Draw a bounding box around every parasitised red blood cell.
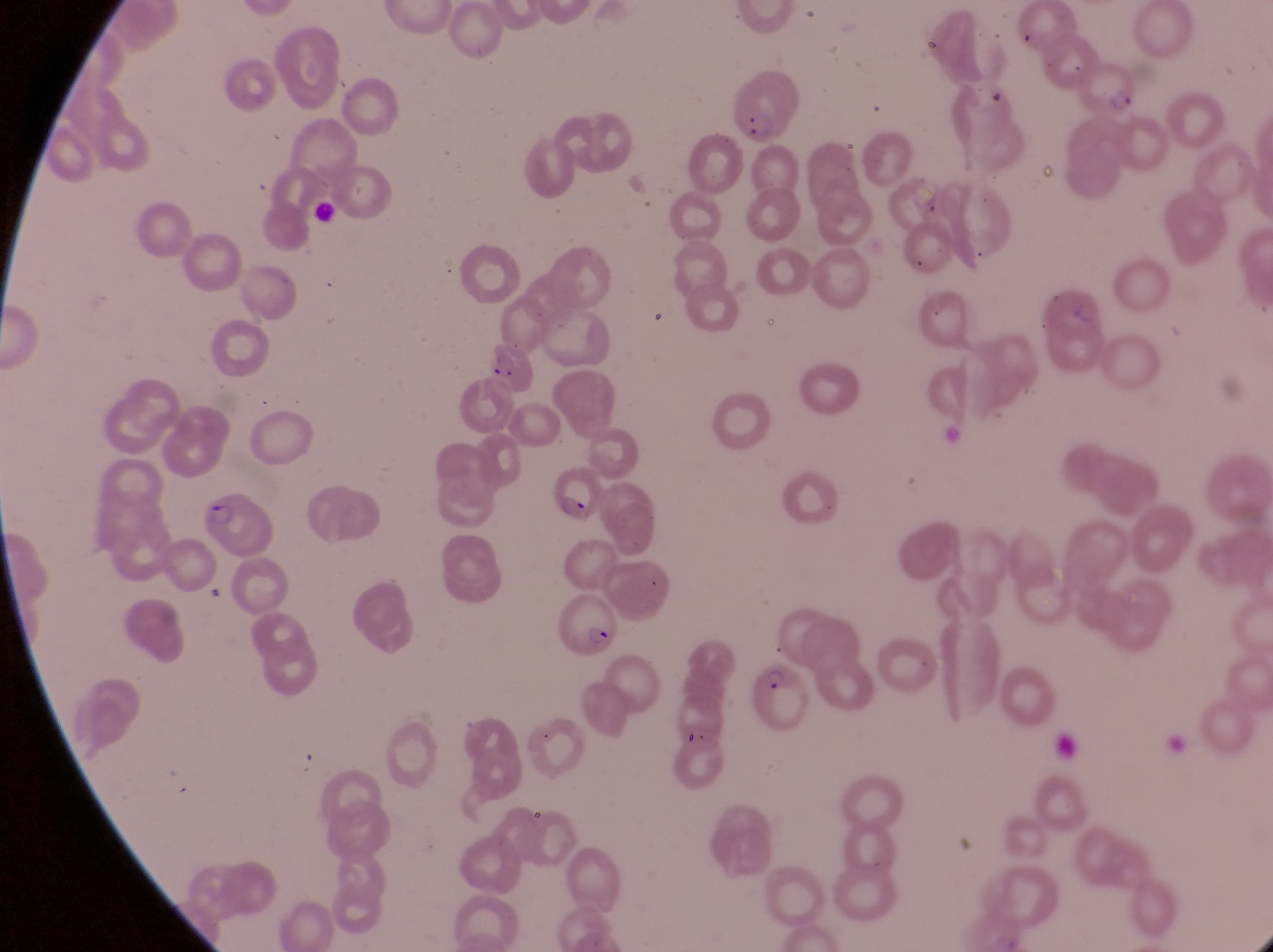
Approximate bounding boxes as left top right bottom in pixels.
Parasitised red blood cells: 1068 55 1138 125; 729 65 796 140; 481 335 539 398; 556 460 604 532; 197 492 280 566; 552 586 624 660; 751 662 818 755.

magnification = 1000x
country = Uganda
preparation = thin blood smear
capture = smartphone photograph through the eyepiece of an Olympus CX-23 microscope
artifact (platelet-like body, stain precipitate, or debris) locations = approximate bounding boxes as left top right bottom in pixels: 304 197 344 230
field of view = single
image size = 1273×952 pixels